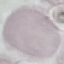
{
  "result": "no malaria parasites seen",
  "stain": "Giemsa",
  "preparation": "thin smear",
  "capture": "smartphone through the microscope eyepiece",
  "image_type": "automatically extracted cell patch, resized to 64 × 64 pixels"
}